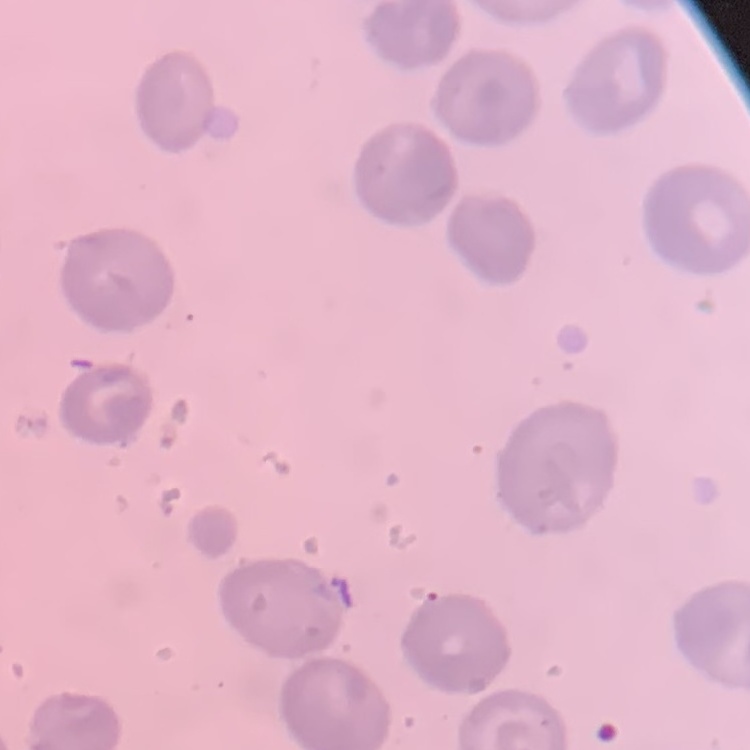

erythrocyte morphology = no rouleaux formation
stain = Field's or Giemsa
preparation = thin blood film
image type = one tile cut from a larger photomicrograph